Name the blood parasite species.
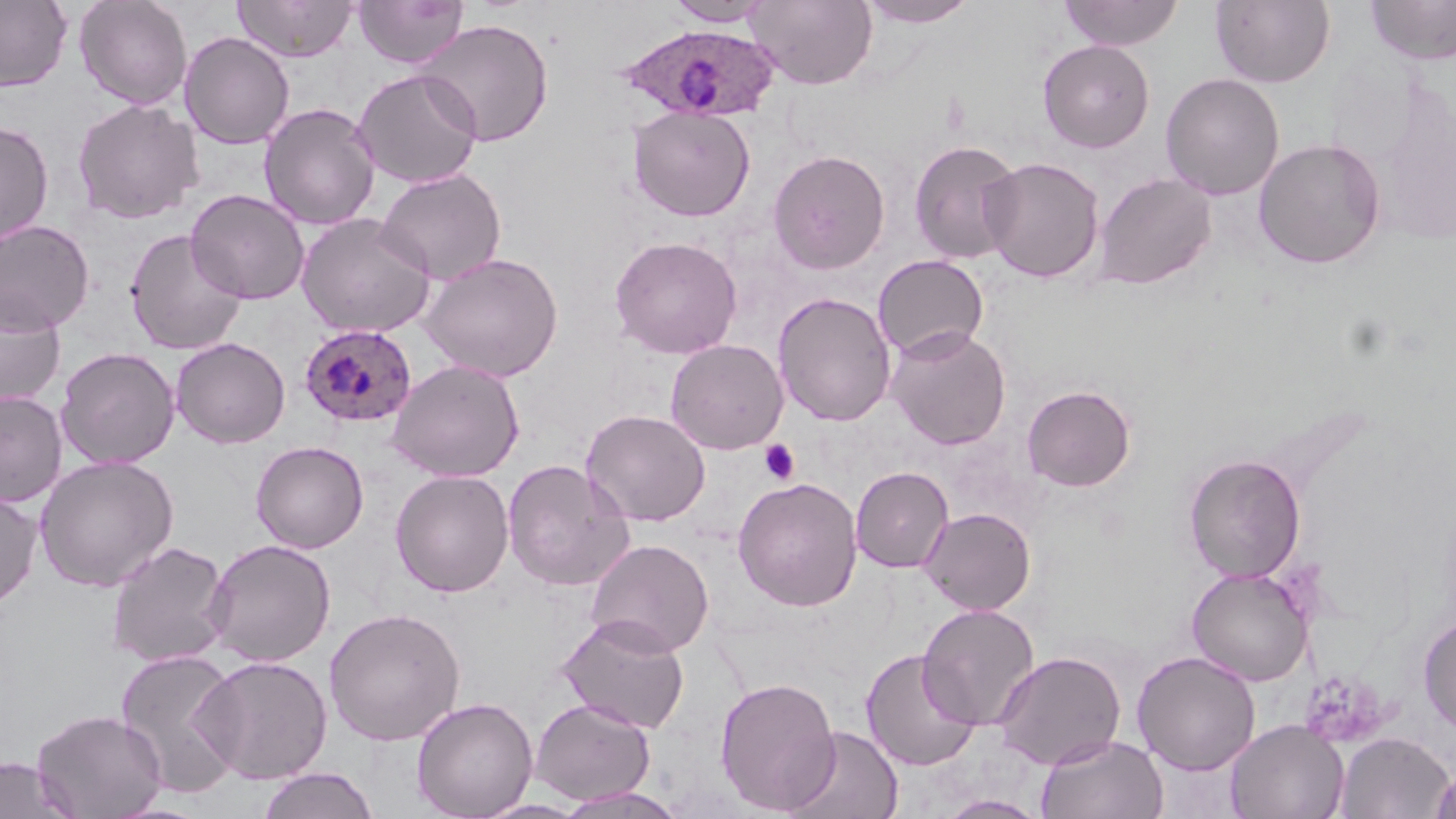
Plasmodium ovale.

{
  "magnification": "1000x",
  "stain": "May-Grünwald-Giemsa",
  "plasmodium_ovale_infected_red_blood_cell_locations": "approximate bounding boxes as named x1/y1/x2/y2 corners in pixels: (x1=615, y1=23, x2=781, y2=123), (x1=300, y1=324, x2=417, y2=427)",
  "preparation": "thin blood smear",
  "modality": "optical microscopy",
  "field_of_view": "single",
  "platelet_locations": "approximate bounding boxes as named x1/y1/x2/y2 corners in pixels: (x1=759, y1=439, x2=800, y2=484)",
  "image_size": "1456×819 pixels",
  "uninfected_red_blood_cell_locations": "approximate bounding boxes as named x1/y1/x2/y2 corners in pixels: (x1=74, y1=0, x2=193, y2=109), (x1=233, y1=0, x2=357, y2=62), (x1=353, y1=0, x2=468, y2=69), (x1=745, y1=0, x2=878, y2=90), (x1=1059, y1=0, x2=1184, y2=51), (x1=1365, y1=0, x2=1456, y2=64), (x1=0, y1=1, x2=72, y2=91), (x1=664, y1=1, x2=773, y2=27), (x1=857, y1=1, x2=978, y2=27), (x1=1210, y1=1, x2=1335, y2=87), (x1=416, y1=18, x2=554, y2=147), (x1=179, y1=31, x2=295, y2=150), (x1=1038, y1=39, x2=1155, y2=153), (x1=352, y1=68, x2=483, y2=189), (x1=1160, y1=72, x2=1284, y2=201), (x1=72, y1=97, x2=204, y2=225), (x1=259, y1=103, x2=381, y2=231), (x1=627, y1=105, x2=756, y2=221), (x1=0, y1=120, x2=54, y2=246), (x1=909, y1=138, x2=1024, y2=265), (x1=1253, y1=138, x2=1386, y2=269), (x1=768, y1=149, x2=890, y2=274), (x1=980, y1=156, x2=1104, y2=283), (x1=375, y1=167, x2=507, y2=286), (x1=1093, y1=172, x2=1216, y2=291), (x1=185, y1=188, x2=310, y2=305), (x1=295, y1=213, x2=436, y2=338), (x1=0, y1=219, x2=95, y2=335), (x1=125, y1=228, x2=247, y2=355), (x1=608, y1=235, x2=743, y2=359), (x1=420, y1=252, x2=564, y2=382), (x1=872, y1=254, x2=989, y2=361), (x1=773, y1=292, x2=897, y2=427), (x1=0, y1=293, x2=66, y2=408), (x1=885, y1=325, x2=1011, y2=450), (x1=171, y1=337, x2=291, y2=449), (x1=665, y1=338, x2=788, y2=454), (x1=56, y1=347, x2=180, y2=469), (x1=388, y1=359, x2=525, y2=481), (x1=1022, y1=384, x2=1136, y2=492), (x1=0, y1=391, x2=68, y2=508), (x1=580, y1=409, x2=711, y2=526), (x1=250, y1=441, x2=369, y2=553), (x1=1183, y1=453, x2=1306, y2=583), (x1=34, y1=454, x2=179, y2=592), (x1=501, y1=459, x2=635, y2=592), (x1=850, y1=466, x2=954, y2=573), (x1=389, y1=469, x2=514, y2=597), (x1=732, y1=476, x2=863, y2=611), (x1=0, y1=487, x2=42, y2=611), (x1=920, y1=507, x2=1036, y2=615), (x1=204, y1=538, x2=336, y2=667), (x1=585, y1=538, x2=714, y2=657), (x1=106, y1=540, x2=232, y2=667), (x1=1187, y1=566, x2=1312, y2=686), (x1=917, y1=603, x2=1040, y2=730), (x1=324, y1=607, x2=466, y2=746), (x1=556, y1=615, x2=691, y2=734), (x1=1418, y1=615, x2=1456, y2=733), (x1=113, y1=648, x2=247, y2=798), (x1=860, y1=648, x2=981, y2=771), (x1=992, y1=651, x2=1126, y2=770), (x1=1132, y1=651, x2=1261, y2=775), (x1=195, y1=655, x2=333, y2=784), (x1=714, y1=676, x2=841, y2=814), (x1=411, y1=697, x2=538, y2=818), (x1=530, y1=697, x2=656, y2=806), (x1=31, y1=708, x2=168, y2=819), (x1=1225, y1=718, x2=1349, y2=819), (x1=784, y1=725, x2=904, y2=819), (x1=1335, y1=731, x2=1454, y2=818), (x1=1035, y1=733, x2=1169, y2=819), (x1=0, y1=757, x2=78, y2=819), (x1=1430, y1=762, x2=1456, y2=819), (x1=255, y1=767, x2=381, y2=819), (x1=552, y1=786, x2=689, y2=819), (x1=936, y1=794, x2=1050, y2=818), (x1=475, y1=797, x2=591, y2=818)"
}